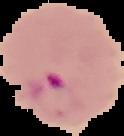
malaria status = parasitized
image size = 124×136 pixels
image type = cell region segmented out of the field of view; surrounding area masked to black
preparation = thin blood smear